Assess this cell for malaria.
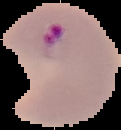

It is parasitized.

{
  "image_type": "cell region segmented out of the field of view; surrounding area masked to black",
  "image_size": "121×130 pixels",
  "preparation": "thin blood smear"
}